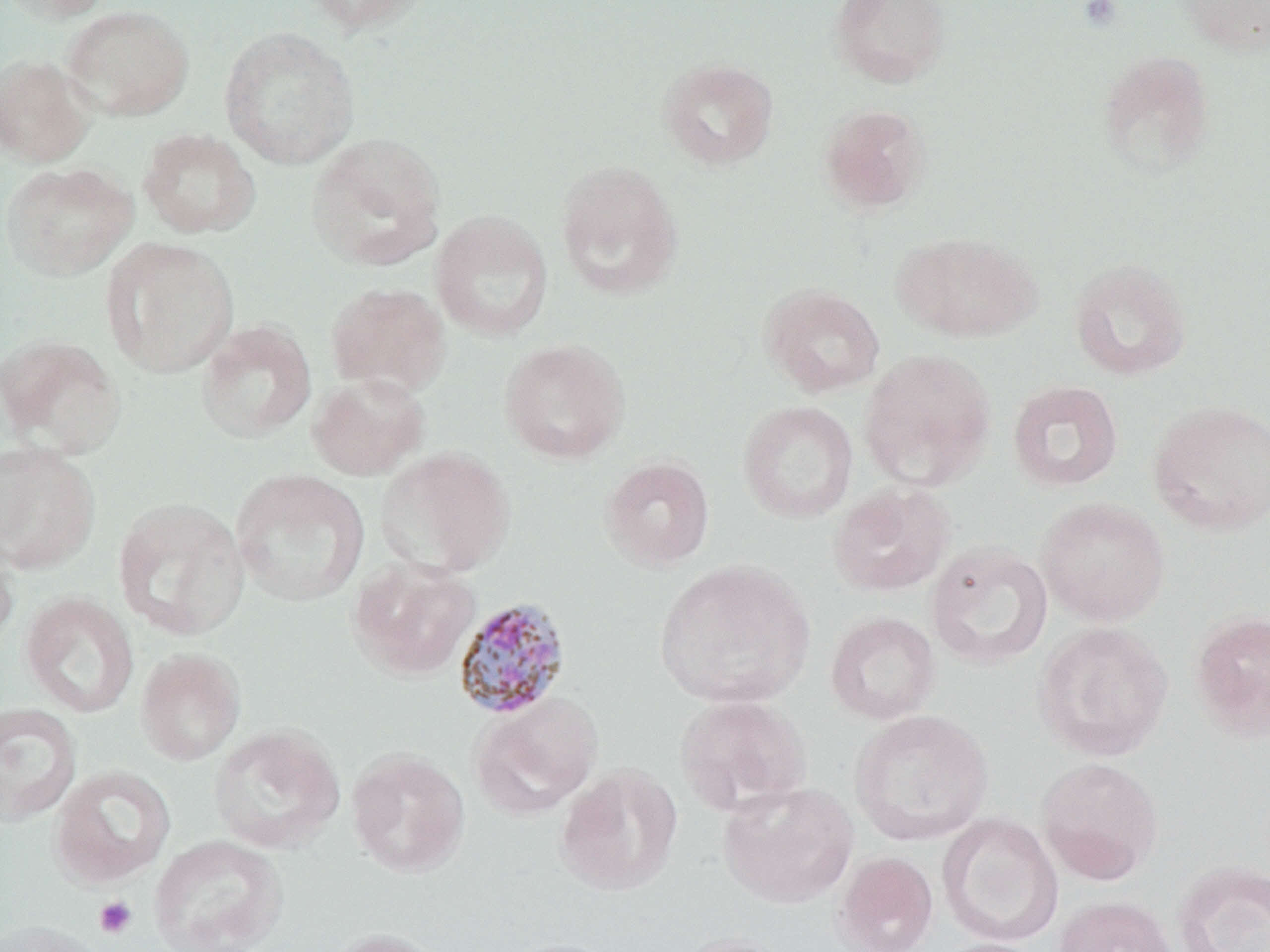 Approximate bounding boxes as (x1, y1, x2, y2) in pixels. Plasmodium malariae-infected red blood cell locations: (452, 597, 572, 721). Uninfected red blood cell locations: (0, 0, 117, 23), (300, 0, 434, 35), (829, 0, 951, 89), (1177, 0, 1270, 56), (62, 5, 194, 121), (219, 26, 360, 170), (1097, 50, 1215, 179), (0, 55, 97, 167), (657, 57, 779, 170), (819, 104, 931, 214), (138, 127, 260, 239), (306, 132, 446, 271), (555, 159, 683, 300), (1, 162, 137, 281), (430, 210, 553, 342), (894, 232, 1042, 343), (101, 237, 240, 379), (1068, 258, 1193, 381), (325, 281, 451, 397), (759, 283, 885, 397), (195, 320, 317, 443), (0, 334, 126, 459), (499, 338, 630, 464), (859, 348, 997, 491), (307, 371, 429, 481), (1007, 379, 1124, 492), (1148, 399, 1270, 536), (737, 400, 859, 523), (0, 440, 101, 574), (376, 446, 516, 578), (599, 456, 715, 571), (230, 469, 369, 607), (827, 481, 956, 597), (1035, 496, 1170, 626), (112, 497, 250, 641), (0, 529, 20, 656), (925, 542, 1053, 670), (348, 558, 480, 681), (653, 559, 815, 710), (20, 592, 139, 718), (1189, 609, 1270, 742), (825, 611, 940, 725), (1033, 621, 1173, 761), (135, 648, 246, 766), (469, 693, 603, 820), (674, 694, 812, 817), (0, 702, 82, 827), (849, 708, 994, 845), (207, 724, 345, 854), (346, 747, 470, 877), (1035, 756, 1164, 884), (49, 764, 176, 888), (554, 764, 682, 896), (717, 780, 860, 908), (938, 812, 1063, 947), (149, 834, 288, 952), (832, 851, 938, 951), (1171, 861, 1270, 952), (1052, 895, 1178, 952), (0, 919, 109, 952), (323, 927, 450, 952), (670, 931, 796, 952), (498, 937, 624, 952), (931, 938, 1051, 952). Platelet locations: (1078, 0, 1123, 30), (94, 896, 137, 939). Slide-level diagnosis: Plasmodium malariae. Light microscopy. Thin blood film. Captured at 1000x magnification. Image is 1270×952 pixels. May-Grünwald-Giemsa stain. Single field of view.